Mark where platelets are.
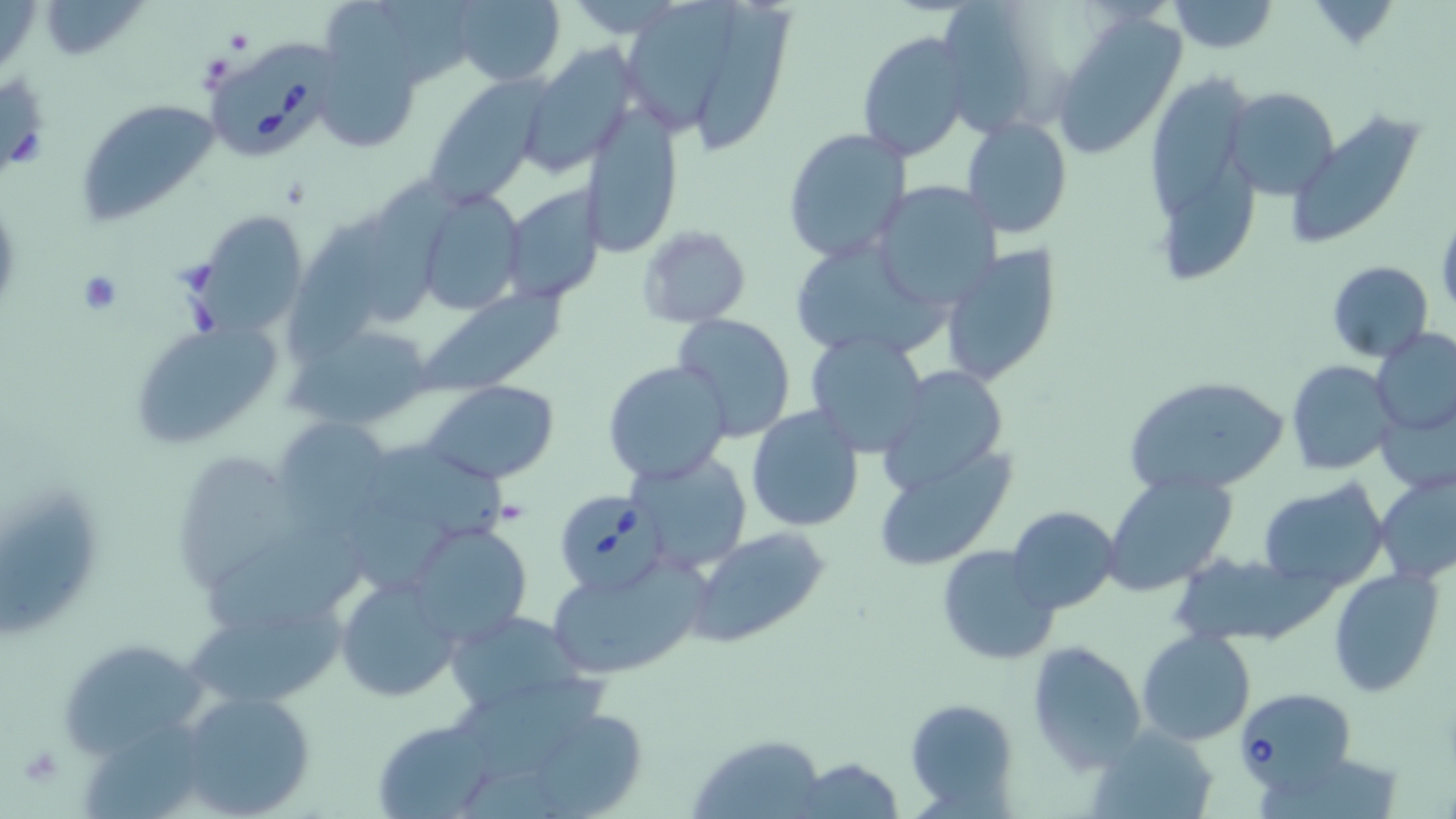
Approximate bounding boxes as (x1, y1, x2, y2) in pixels.
Platelets: (497, 499, 530, 525), (17, 744, 64, 788).

Uninfected red blood cell locations: (41, 0, 146, 61), (445, 0, 567, 87), (626, 0, 736, 134), (693, 0, 798, 153), (939, 0, 1040, 134), (1167, 0, 1278, 53), (1050, 14, 1186, 158), (314, 29, 426, 155), (856, 30, 973, 163), (518, 44, 636, 178), (1144, 60, 1258, 288), (424, 80, 545, 205), (1226, 85, 1340, 200), (76, 98, 226, 225), (579, 102, 682, 256), (1287, 109, 1424, 246), (959, 116, 1073, 241), (782, 127, 912, 263), (361, 172, 476, 327), (871, 182, 1001, 309), (499, 184, 605, 302), (410, 188, 528, 316), (185, 210, 309, 338), (288, 214, 385, 353), (636, 223, 752, 330), (797, 243, 957, 363), (939, 246, 1063, 388), (1325, 260, 1434, 361), (421, 288, 568, 394), (673, 313, 796, 442), (127, 319, 288, 448), (291, 324, 437, 430), (1374, 329, 1456, 435), (804, 331, 931, 456), (603, 360, 732, 486), (1286, 360, 1395, 475), (877, 366, 1009, 497), (1121, 372, 1292, 497), (424, 381, 561, 485), (1379, 399, 1455, 495), (747, 406, 864, 531), (271, 418, 396, 528), (375, 442, 507, 550), (873, 447, 1017, 572), (627, 450, 752, 571), (181, 454, 303, 586), (1102, 471, 1238, 595), (1375, 471, 1456, 585), (1260, 480, 1388, 589), (0, 488, 109, 650), (1008, 505, 1120, 614), (405, 523, 532, 647), (687, 526, 833, 649), (202, 527, 375, 641), (938, 545, 1058, 666), (1177, 554, 1326, 647), (546, 559, 707, 679), (1329, 568, 1443, 697), (334, 574, 462, 702), (442, 608, 591, 720), (181, 621, 357, 705), (1137, 630, 1256, 746), (61, 638, 209, 755), (1026, 639, 1147, 771), (455, 674, 619, 777), (178, 688, 317, 819), (906, 697, 1018, 813), (535, 716, 643, 819), (370, 717, 505, 819), (1090, 725, 1219, 818), (691, 733, 828, 818), (788, 757, 908, 817). Babesia divergens-infected red blood cell locations: (209, 38, 343, 166), (558, 492, 665, 590), (1236, 687, 1355, 794). Slide-level diagnosis: Babesia divergens. Light microscopy. Captured at 1000x magnification. Image is 1456×819 pixels. Thin blood smear. Single field of view. May-Grünwald-Giemsa stain.